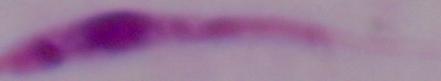

Summary:
  - Magnification: 1000x
  - Modality: photomicrograph
  - Identification: Leishmania